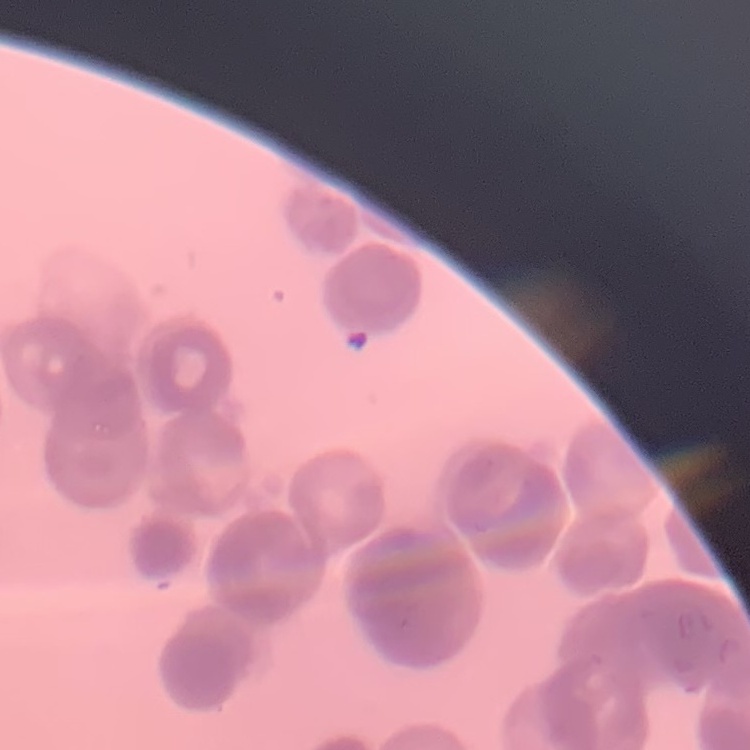

red_blood_cell_morphology: rouleaux formation
image_type: square crop of a larger photomicrograph
stain: Field's or Giemsa
preparation: thin peripheral smear